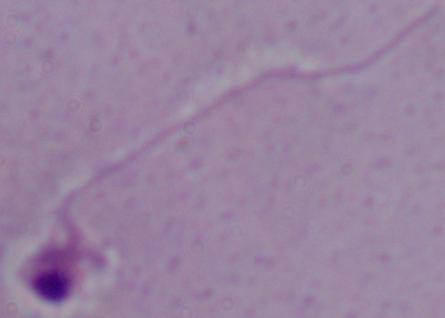 A Leishmania parasite is seen. Micrograph. 1000x magnification.